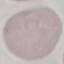
Result: no malaria parasites seen. Thin blood film. Cell patch, automatically extracted from a larger field of view and resized to 64 × 64 pixels. Giemsa-stained preparation. Photographed with a smartphone camera at the microscope eyepiece.